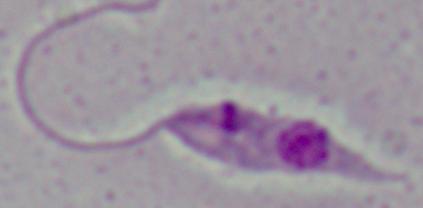

Summary:
  - Magnification: 1000x
  - Modality: photomicrograph
  - Identification: Leishmania